Locate every Plasmodium parasite.
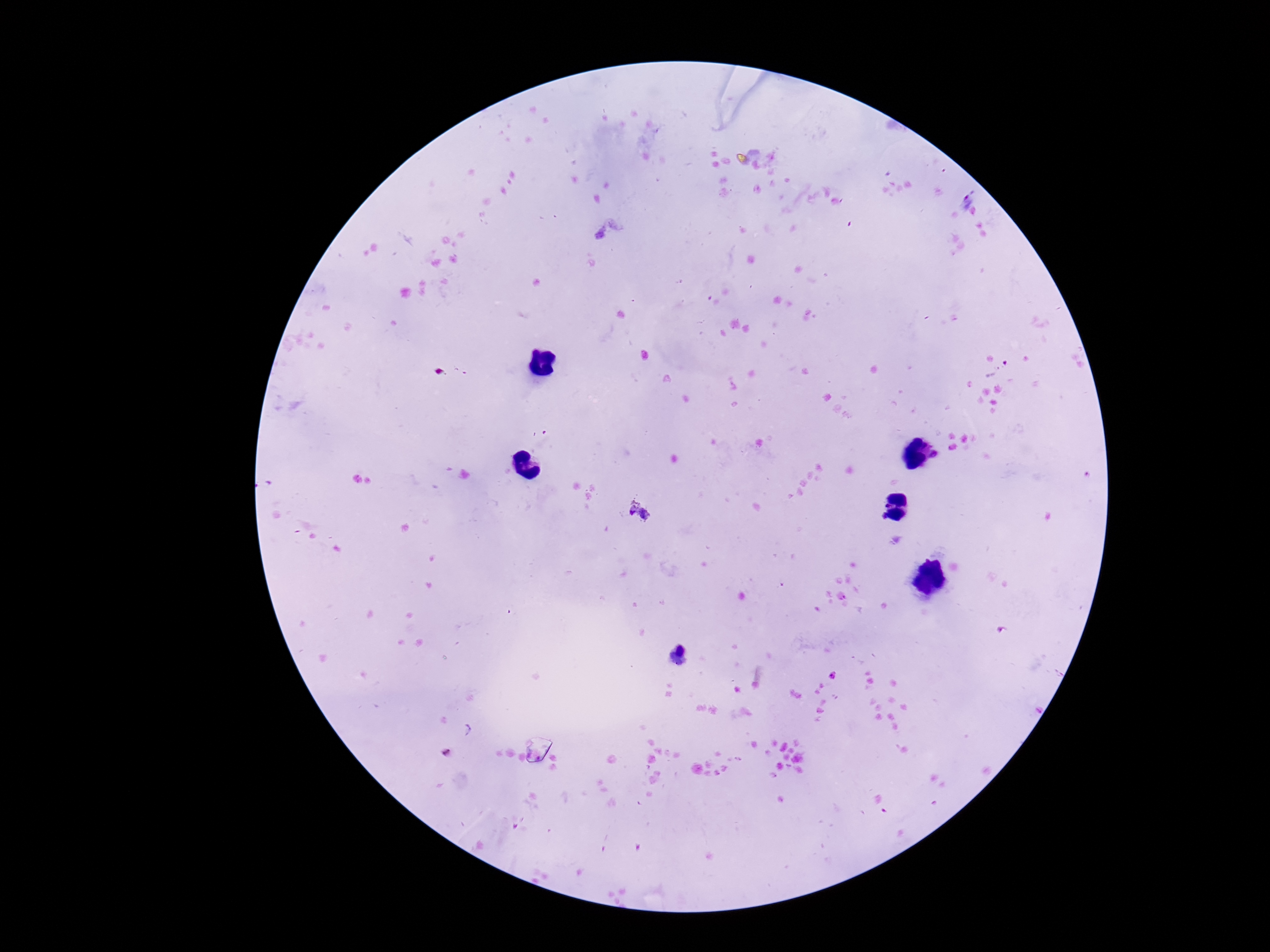
Approximate centers as [x, y] in pixels.
Plasmodium parasites: [996, 368], [1089, 477], [639, 510].

capture = smartphone camera through the microscope eyepiece
patient malaria status = infected
image size = 1270×952 pixels
magnification = 100x
field of view = single
stain = Giemsa
preparation = thick blood smear